Name the blood parasite species.
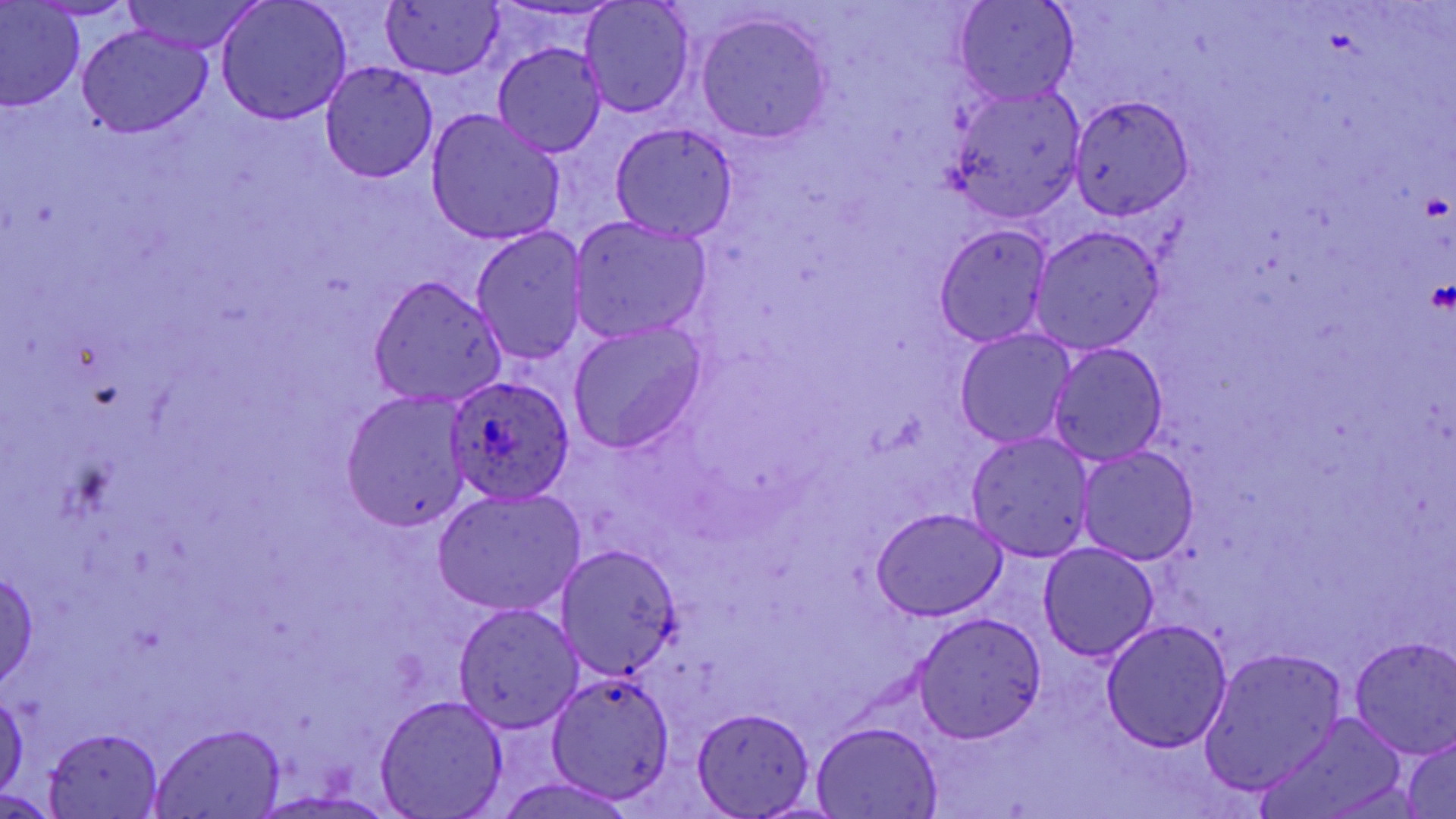
Plasmodium ovale.

Approximate bounding boxes as (x1,y1)-(x2,y2) corner pairs in pixels. Plasmodium ovale-infected red blood cell locations: (443,373)-(574,505). Platelet locations: (1418,189)-(1451,221), (1425,277)-(1455,316). Uninfected red blood cell locations: (120,0)-(264,53), (953,0)-(1078,107), (580,1)-(696,119), (30,2)-(137,20), (216,2)-(351,125), (381,3)-(502,79), (1,4)-(83,109), (696,13)-(832,143), (77,26)-(212,136), (492,43)-(607,158), (321,64)-(438,183), (947,87)-(1085,224), (1068,95)-(1195,220), (426,109)-(566,246), (609,122)-(739,242), (569,216)-(714,344), (932,224)-(1053,346), (1030,227)-(1163,353), (471,228)-(588,365), (370,277)-(507,406), (567,320)-(708,455), (955,328)-(1075,448), (1047,342)-(1169,467), (342,390)-(468,534), (965,432)-(1097,561), (1077,446)-(1199,565), (435,487)-(586,616), (871,508)-(1007,621), (556,543)-(681,677), (1037,543)-(1159,661), (0,568)-(40,688), (452,603)-(585,734), (914,612)-(1046,743), (1102,620)-(1232,752), (1348,636)-(1456,758), (1201,646)-(1348,794), (544,672)-(677,801), (0,691)-(27,800), (375,696)-(509,817), (691,707)-(817,819), (1261,713)-(1408,819), (810,722)-(944,817), (150,724)-(286,818), (42,726)-(166,818), (1401,734)-(1456,818), (491,776)-(641,819), (252,790)-(392,817), (0,791)-(60,816). Thin blood smear. Image is 1456×819 pixels. 1000x magnification. May-Grünwald-Giemsa-stained preparation. Light microscopy. Single field of view.